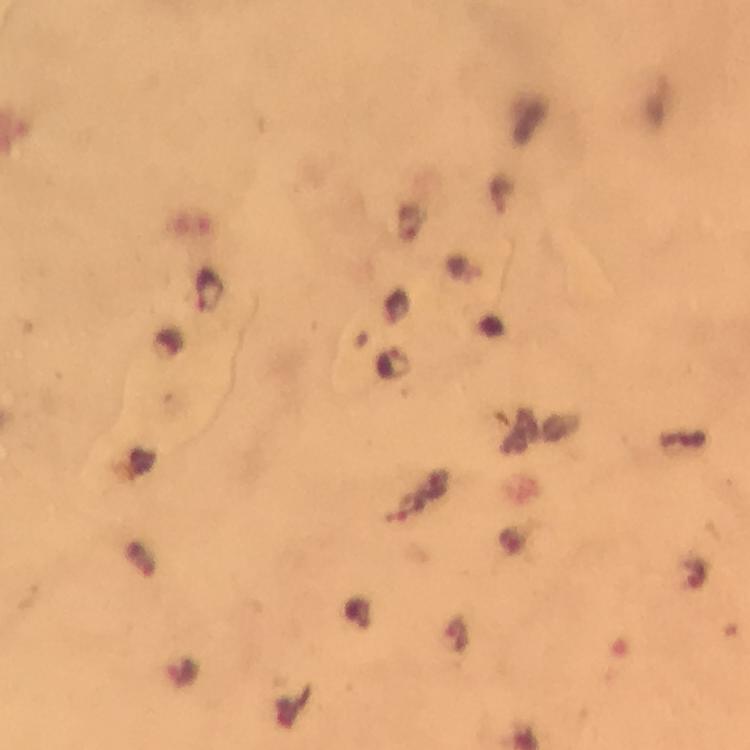

Approximate centers as [x, y] in pixels.
Summary:
  - Malaria parasite locations: [210, 289]
  - Preparation: thick smear
  - Cropped from: one field of view
  - Stain: Giemsa
  - Magnification: 100x
  - Capture: smartphone photograph through a microscope
  - Immersion oil: used
  - Context: from a diagnostic examination for malaria
  - Image size: 750×750 pixels